Locate every Plasmodium parasite.
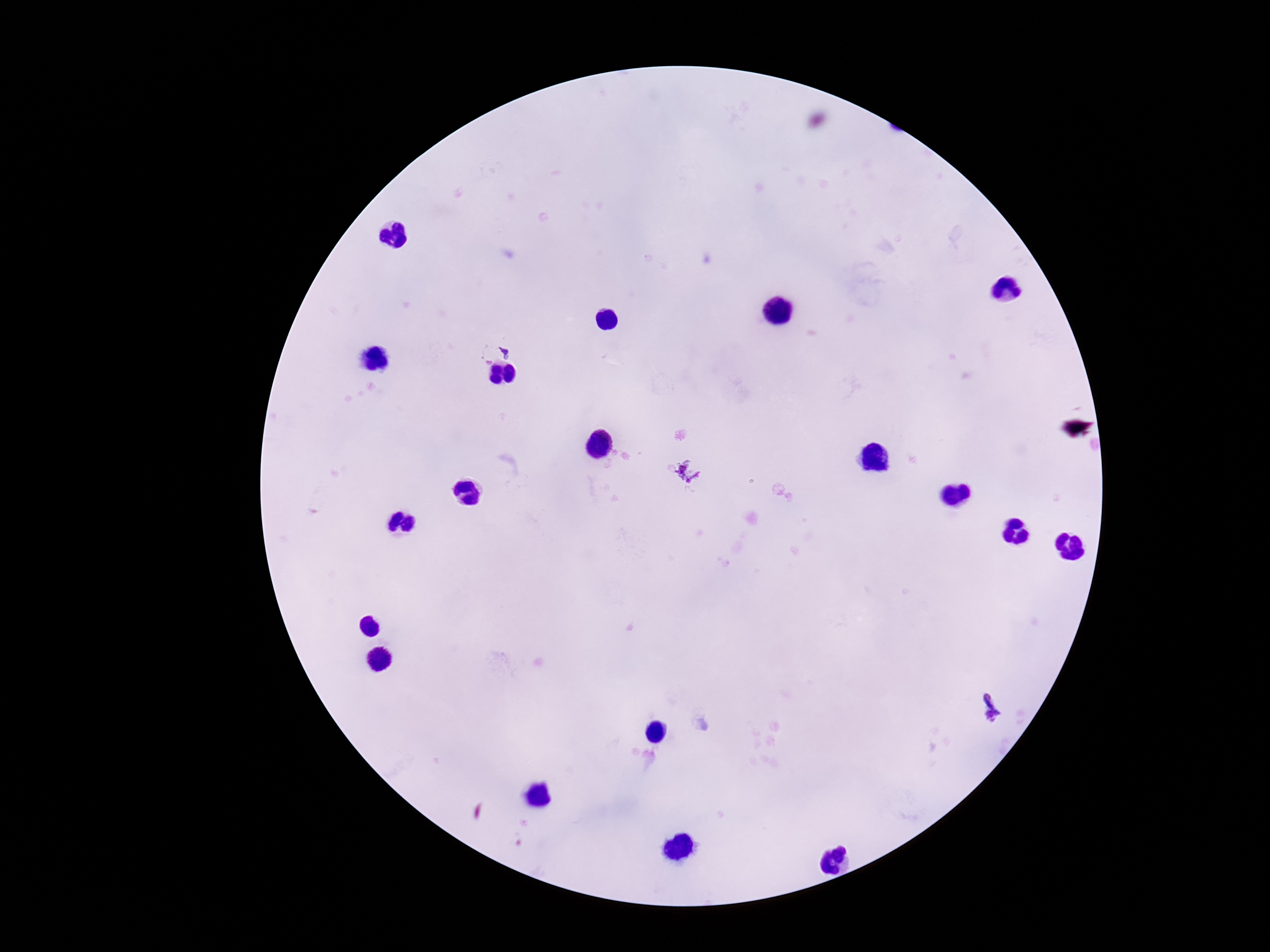
Approximate object centers, in pixels from the top-left corner.
Plasmodium parasites: (x=507, y=351), (x=690, y=471), (x=992, y=709).

Summary:
  - Image size: 1270×952 pixels
  - Field of view: single
  - Preparation: thick blood film
  - Capture: smartphone camera through the microscope eyepiece
  - Stain: Giemsa
  - Magnification: 100x
  - Patient malaria status: infected